Describe the morphology of the red blood cells.
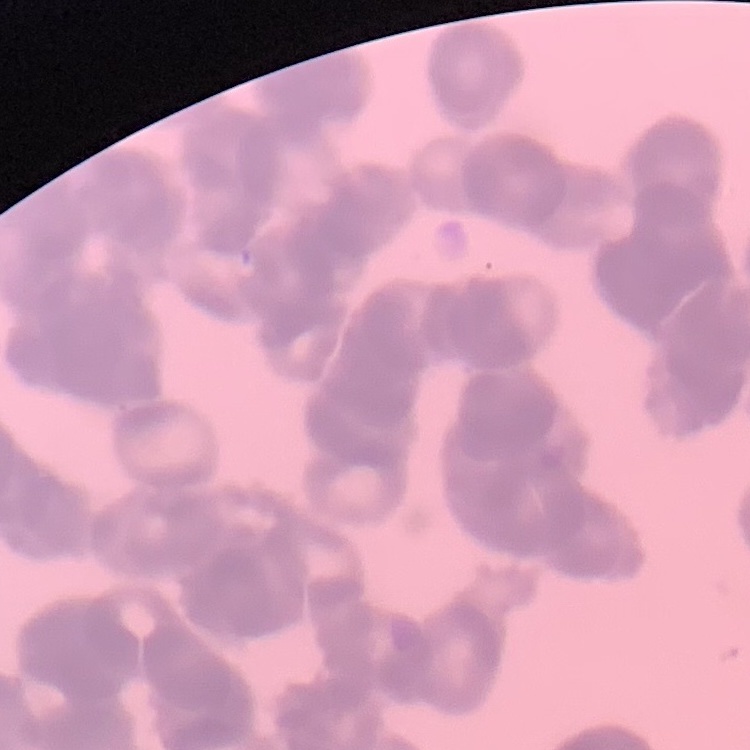
Rouleaux formation.

image type = one tile cut from a larger photomicrograph
stain = Field's or Giemsa
preparation = thin peripheral smear